Classify this cell by malaria status.
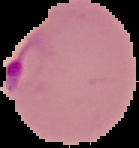
Parasitized.

image size = 139×148 pixels
image type = segmented cell region with the area outside set to black
preparation = thin blood smear